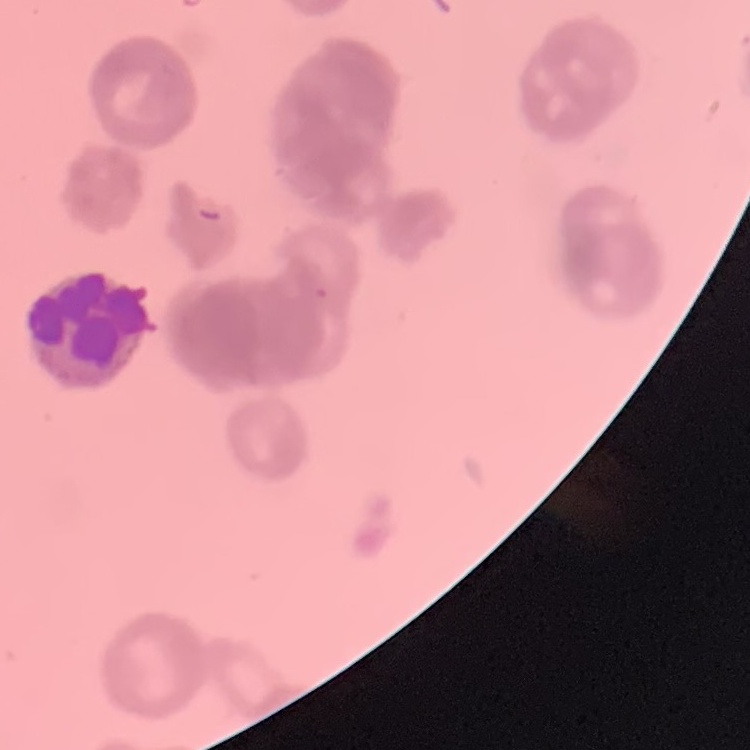
{
  "erythrocyte_morphology": "rouleaux formation",
  "preparation": "thin blood film",
  "image_type": "one tile cut from a larger photomicrograph",
  "stain": "Field's or Giemsa"
}